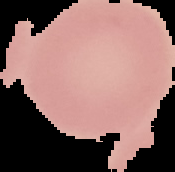

Summary:
  - Image size: 175×172 pixels
  - Image type: segmented cell region with the area outside set to black
  - Preparation: thin blood smear
  - Malaria status: uninfected